Assess for malaria.
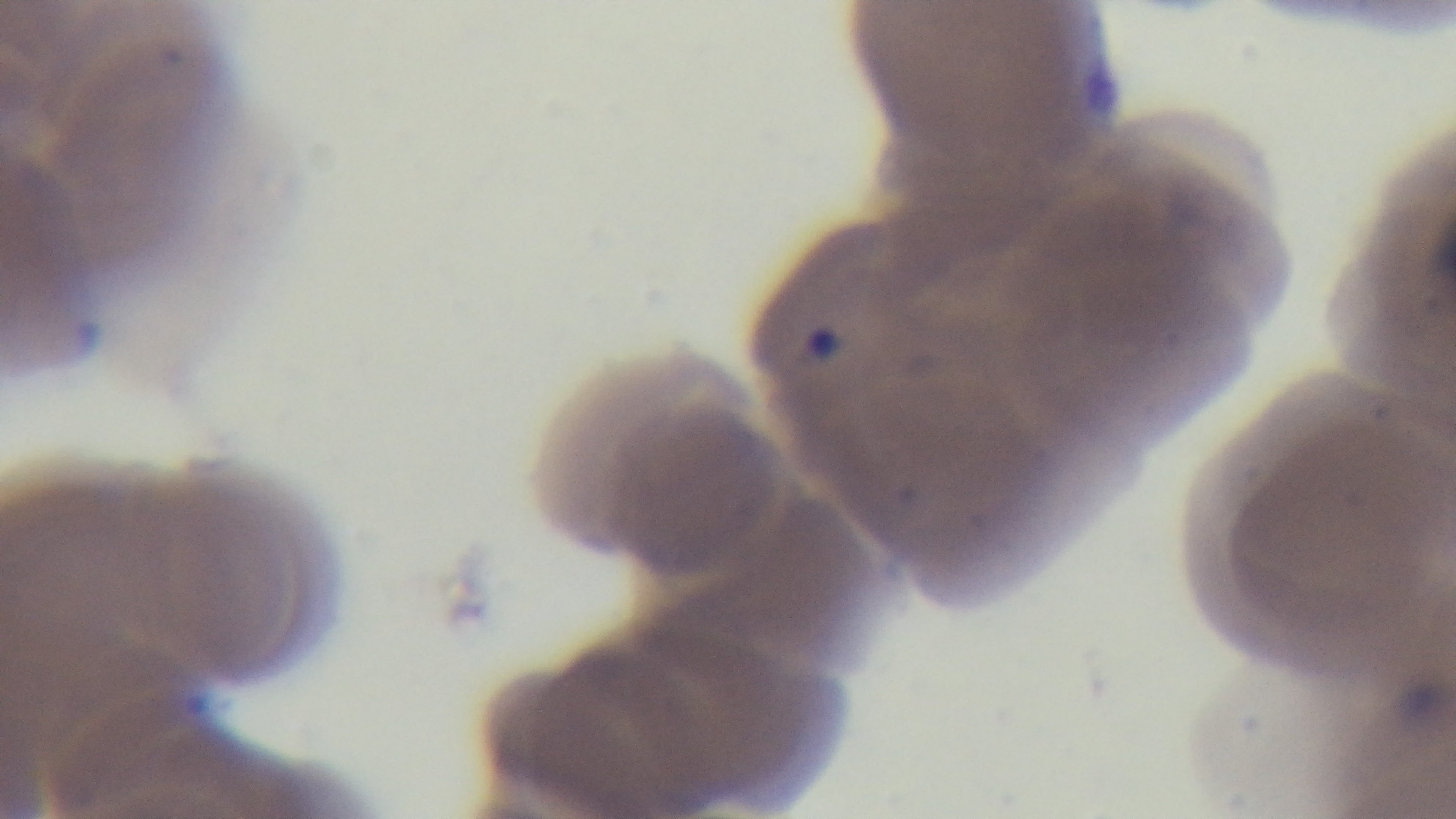

Infected.

stain = Giemsa
capture = mounted 4K digital camera
field of view = single
objective = 100x oil immersion
preparation = thin blood film
modality = light microscopy